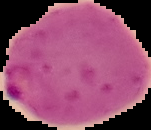 Image is 151×130 pixels. From a thin blood smear. Malaria status: parasitized. Segmented cell region on a black background.